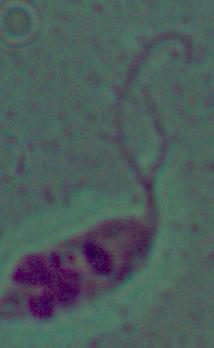

Summary:
  - Identification: Leishmania
  - Magnification: 1000x
  - Modality: photomicrograph